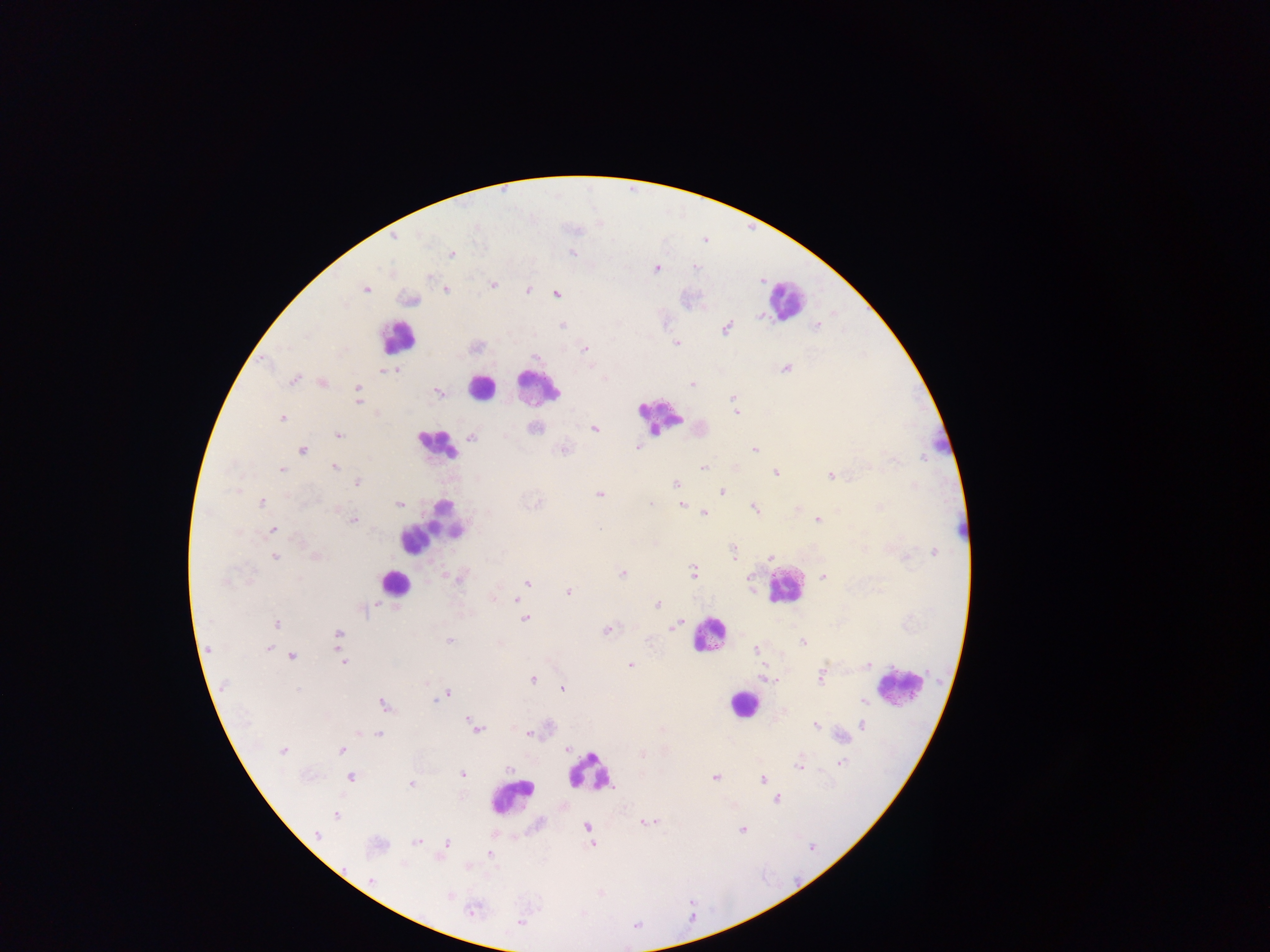
leukocyte_locations: 'approximate centers as {x, y} in pixels: {788, 299}, {397, 337}, {482, 386}, {538, 387}, {660, 415}, {944, 443}, {437, 445}, {432, 525}, {966, 530}, {393, 583}, {783, 586}, {709, 636}, {904, 683}, {743, 704}, {591, 772}, {512, 797}'
plasmodium_parasite_locations: 'approximate centers as {x, y} in pixels: {394, 238}, {571, 253}, {451, 254}, {696, 268}, {656, 269}, {429, 277}, {493, 284}, {366, 289}, {446, 289}, {528, 290}, {556, 294}, {410, 300}, {759, 316}, {562, 325}, {817, 325}, {727, 328}, {676, 343}, {585, 349}, {534, 358}, {786, 368}, {382, 371}, {387, 371}, {396, 371}, {603, 377}, {294, 380}, {322, 383}, {692, 384}, {358, 387}, {438, 393}, {733, 398}, {358, 402}, {735, 413}, {282, 418}, {534, 428}, {594, 428}, {338, 435}, {471, 437}, {637, 446}, {563, 449}, {755, 449}, {302, 450}, {335, 467}, {735, 467}, {703, 468}, {281, 469}, {776, 473}, {829, 476}, {357, 483}, {676, 483}, {722, 492}, {599, 494}, {262, 503}, {399, 504}, {651, 504}, {682, 505}, {879, 507}, {754, 508}, {797, 509}, {704, 512}, {818, 520}, {353, 521}, {273, 530}, {933, 551}, {732, 552}, {316, 556}, {275, 557}, {771, 557}, {906, 558}, {694, 572}, {622, 573}, {823, 577}, {298, 578}, {225, 581}, {527, 582}, {568, 592}, {494, 599}, {516, 600}, {658, 604}, {363, 609}, {525, 619}, {277, 624}, {675, 626}, {608, 629}, {338, 634}, {449, 640}, {499, 643}, {803, 643}, {268, 649}, {755, 649}, {292, 656}, {344, 662}, {631, 665}, {868, 665}, {762, 677}, {821, 677}, {769, 679}, {533, 680}, {426, 684}, {562, 689}, {297, 690}, {447, 694}, {436, 699}, {862, 700}, {385, 704}, {863, 724}, {816, 725}, {475, 727}, {662, 730}, {529, 733}, {378, 734}, {842, 736}, {567, 748}, {341, 749}, {283, 751}, {643, 754}, {841, 763}, {799, 764}, {509, 769}, {463, 774}, {350, 777}, {714, 778}, {763, 779}, {411, 784}, {777, 800}, {336, 816}, {647, 823}, {587, 827}, {742, 829}, {317, 833}, {417, 842}, {447, 842}, {591, 844}, {489, 854}, {372, 881}, {449, 896}, {473, 911}, {520, 922}'
country: Ghana
capture: mobile-phone photograph through a microscope
field_of_view: single
preparation: thick blood film
image_size: 1270×952 pixels